Assess this cell for malaria.
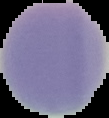
Uninfected.

Image is 109×118 pixels. From a thin blood smear. Cell region segmented out of the field of view; the surrounding area is masked to black.